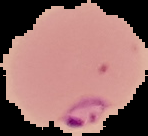

Image is 148×136 pixels. Cell region segmented out of the field of view; the surrounding area is masked to black. From a thin blood smear. Malaria status: parasitized.